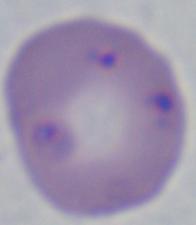
Summary:
  - Identification: Babesia
  - Modality: micrograph
  - Magnification: 1000x